Assess for malaria.
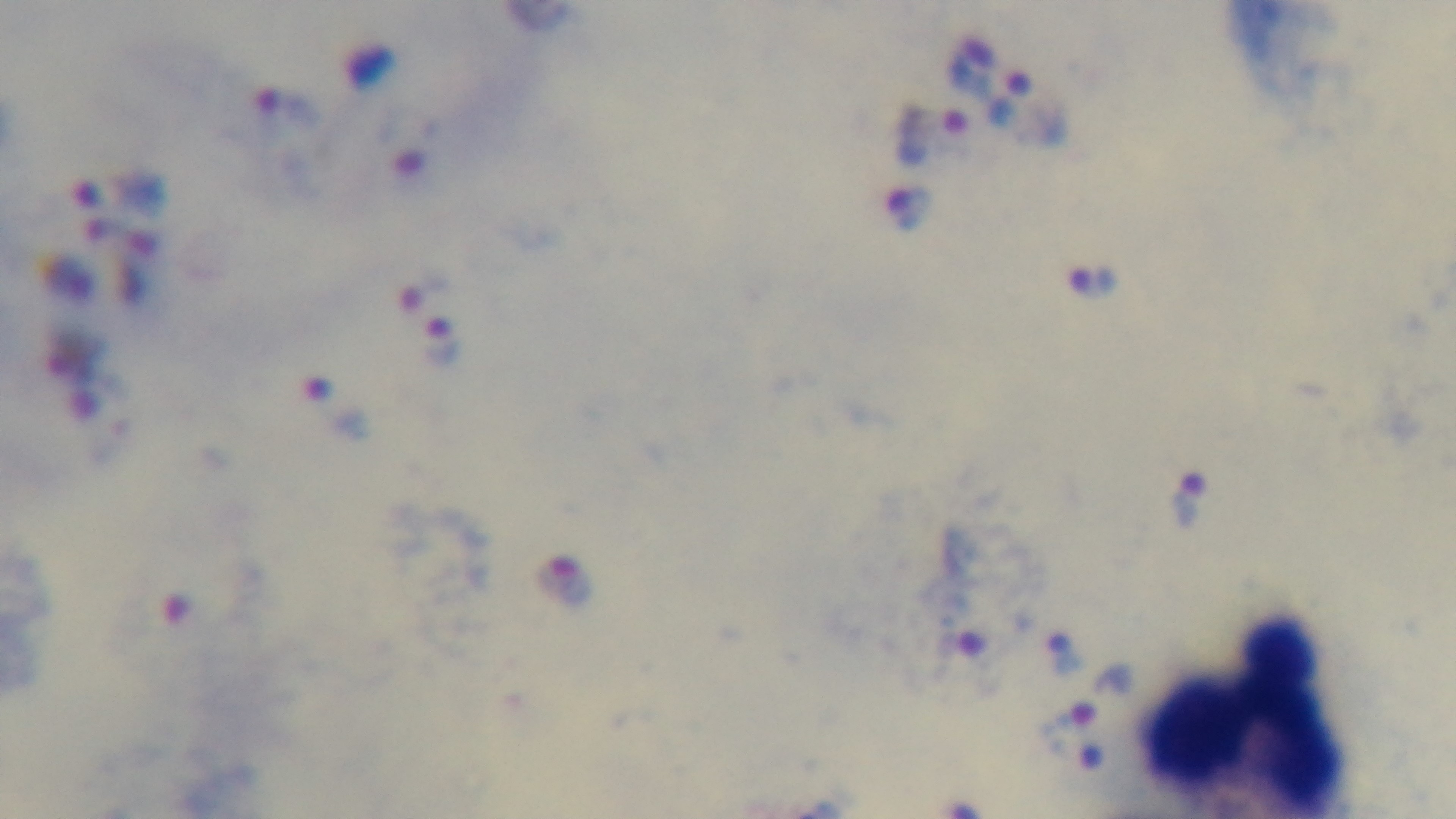

Infected.

stain: Giemsa
field_of_view: single
capture: mounted 4K digital camera
preparation: thick smear
modality: light microscopy
objective: 100x oil immersion